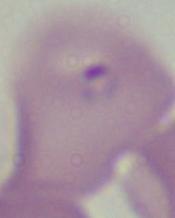

magnification = 1000x
modality = photomicrograph
identification = Babesia